Report the malaria status of this cell.
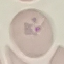

It is parasitized.

Thin blood film. Giemsa stain. Cell patch, automatically extracted from a larger field of view and resized to 64 × 64 pixels. Photographed with a smartphone camera at the microscope eyepiece.